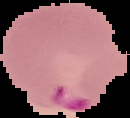
image type = segmented cell region with the area outside set to black
preparation = thin blood smear
image size = 130×118 pixels
result = malaria parasites identified